Report the malaria status of this cell.
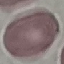
It is uninfected.

stain = Giemsa
image type = automatically extracted cell patch, resized to 64 × 64 pixels
preparation = thin smear
capture = smartphone camera at the microscope eyepiece